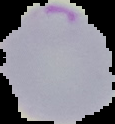

preparation = thin blood smear
image type = cell region segmented out of the field of view; surrounding area masked to black
result = Plasmodium parasites identified
image size = 115×124 pixels